Name the parasite shown.
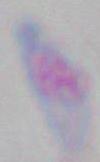
Toxoplasma gondii.

Summary:
  - Modality: photomicrograph
  - Magnification: 1000x